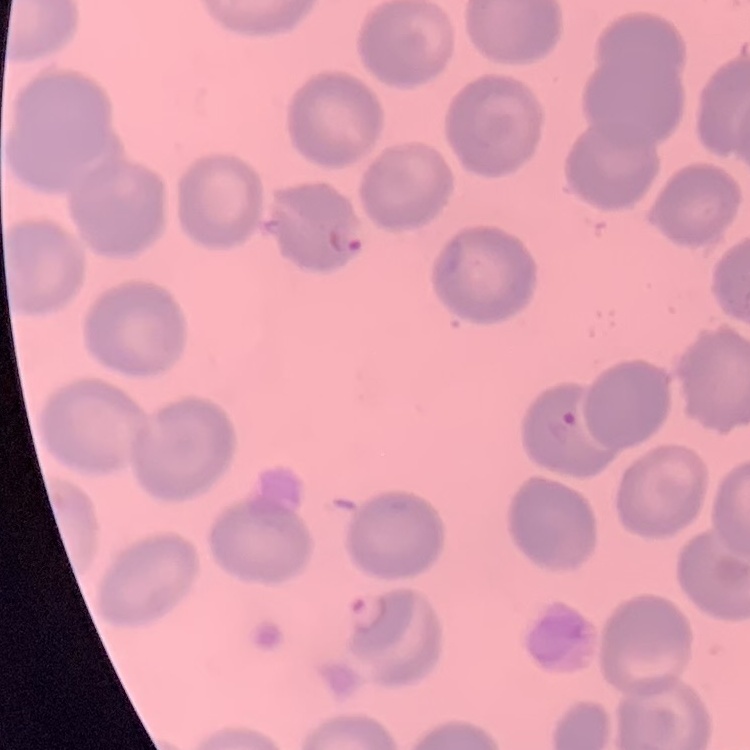
Summary:
  - Red blood cell morphology: no rouleaux formation
  - Stain: Field's or Giemsa
  - Image type: one tile cut from a larger photomicrograph
  - Preparation: thin blood smear